Classify this cell by malaria status.
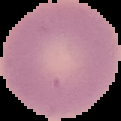
Uninfected.

Image is 121×121 pixels. From a thin blood smear. Cell region segmented out of the field of view; the surrounding area is masked to black.